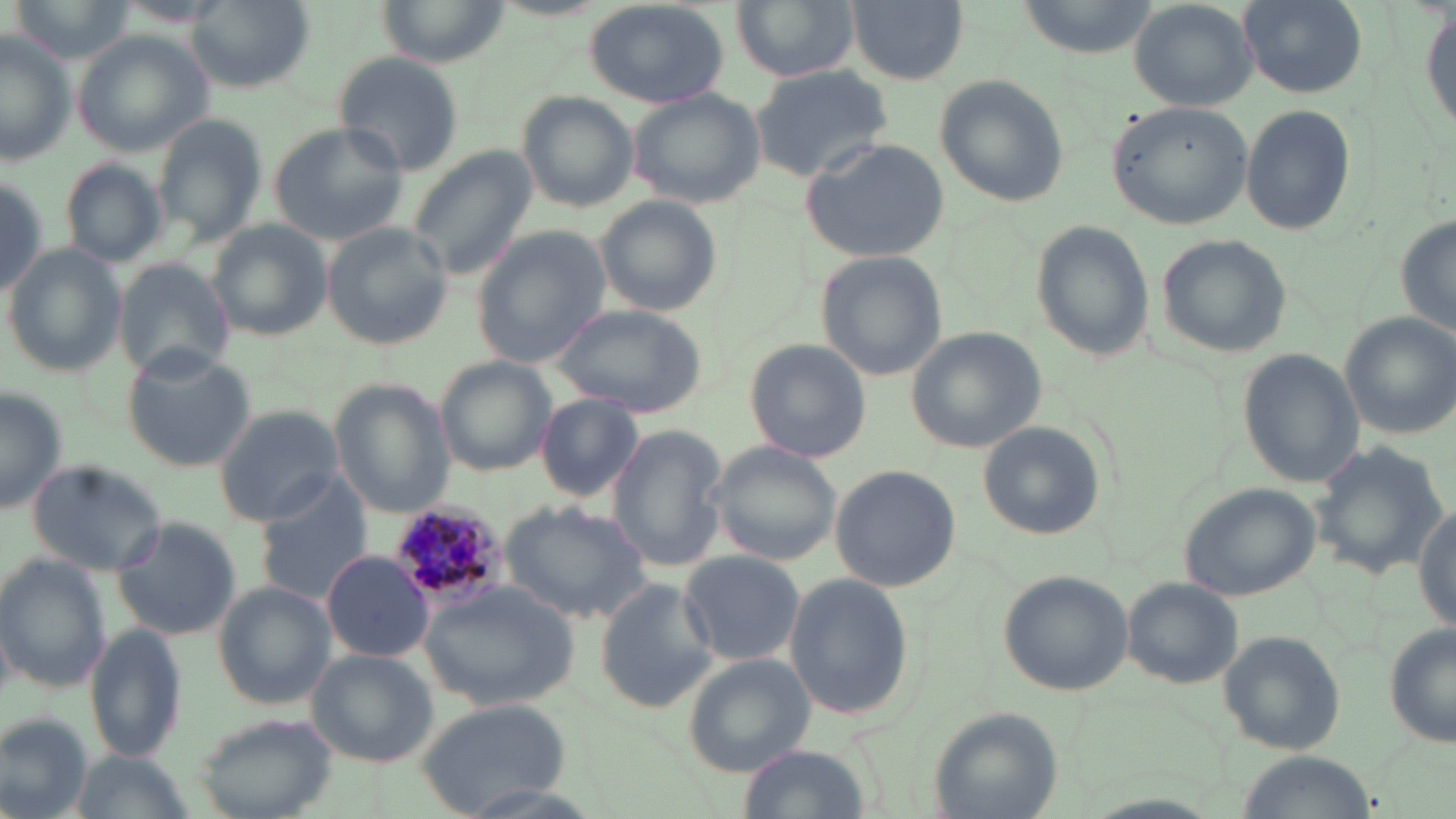

slide-level diagnosis = Plasmodium malariae
modality = light microscopy
stain = May-Grünwald-Giemsa
image size = 1456×819 pixels
field of view = single
preparation = thin blood smear
Plasmodium malariae-infected red blood cell locations = approximate bounding boxes as (x1, y1, x2, y2) in pixels: (385, 501, 513, 611)
magnification = 1000x
uninfected red blood cell locations = approximate bounding boxes as (x1, y1, x2, y2) in pixels: (188, 0, 314, 90), (585, 0, 731, 110), (731, 0, 861, 82), (844, 0, 968, 85), (1015, 0, 1157, 59), (1422, 0, 1456, 142), (1130, 1, 1261, 109), (1240, 1, 1365, 97), (381, 2, 505, 64), (71, 30, 212, 157), (0, 33, 75, 165), (331, 50, 464, 176), (749, 65, 893, 181), (934, 73, 1072, 207), (626, 87, 766, 210), (517, 92, 639, 210), (1106, 98, 1254, 230), (1241, 105, 1356, 236), (151, 115, 263, 244), (270, 120, 413, 245), (802, 137, 950, 264), (405, 144, 537, 281), (60, 160, 168, 269), (0, 172, 50, 296), (594, 194, 723, 318), (1396, 213, 1456, 342), (205, 220, 332, 340), (1031, 220, 1155, 363), (323, 223, 458, 350), (473, 226, 608, 367), (1155, 234, 1292, 357), (5, 246, 123, 374), (817, 250, 949, 381), (113, 258, 231, 383), (553, 304, 707, 417), (1340, 312, 1456, 438), (906, 327, 1047, 455), (743, 339, 873, 465), (126, 349, 258, 469), (1239, 351, 1363, 487), (436, 358, 556, 476), (331, 382, 455, 519), (0, 389, 68, 516), (534, 392, 645, 503), (214, 404, 342, 524), (977, 420, 1106, 542), (606, 424, 728, 573), (1307, 441, 1447, 580), (706, 442, 847, 566), (26, 460, 169, 576), (831, 462, 960, 592), (253, 475, 374, 610), (1179, 482, 1322, 603), (499, 500, 652, 621), (1414, 503, 1455, 628), (111, 517, 237, 641), (321, 549, 434, 661), (679, 550, 804, 667), (2, 557, 111, 694), (998, 570, 1136, 695), (784, 574, 913, 720), (594, 578, 719, 712), (1120, 579, 1242, 689), (214, 583, 334, 711), (418, 583, 577, 710), (86, 624, 186, 763), (1384, 625, 1456, 749), (1221, 631, 1344, 753), (307, 649, 439, 767), (683, 656, 813, 777), (414, 697, 571, 811), (928, 707, 1065, 819), (1, 713, 91, 818), (196, 715, 339, 819), (736, 745, 874, 819), (1240, 751, 1369, 818)